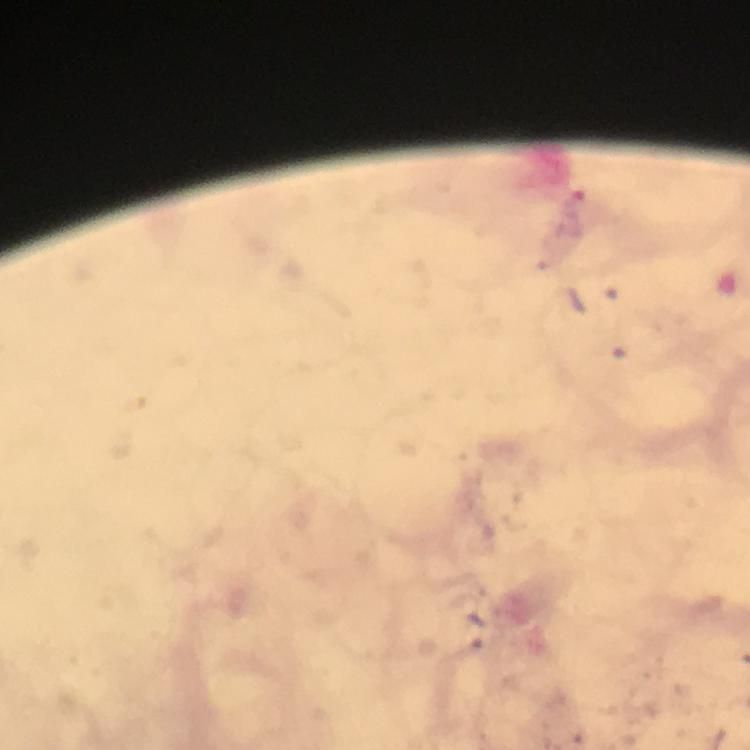

Approximate centers as (x, y) in pixels. Plasmodium parasite locations: (575, 205). From a diagnostic examination for malaria. Thick smear. Smartphone photograph taken through a microscope. Image is 750×750 pixels. Immersion oil was used. At 100x magnification. A crop from one field of view. Giemsa stain.